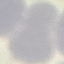
Summary:
  - Malaria status: uninfected
  - Image type: cell patch, automatically extracted from a larger field of view and resized to 64 × 64 pixels
  - Preparation: thin smear
  - Capture: smartphone through the microscope eyepiece
  - Stain: Giemsa